Name the parasite shown.
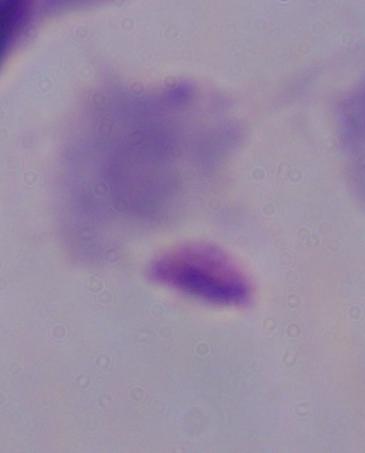

A trichomonad.

Summary:
  - Modality: micrograph
  - Magnification: 1000x